Outline each blood parasite and name the species.
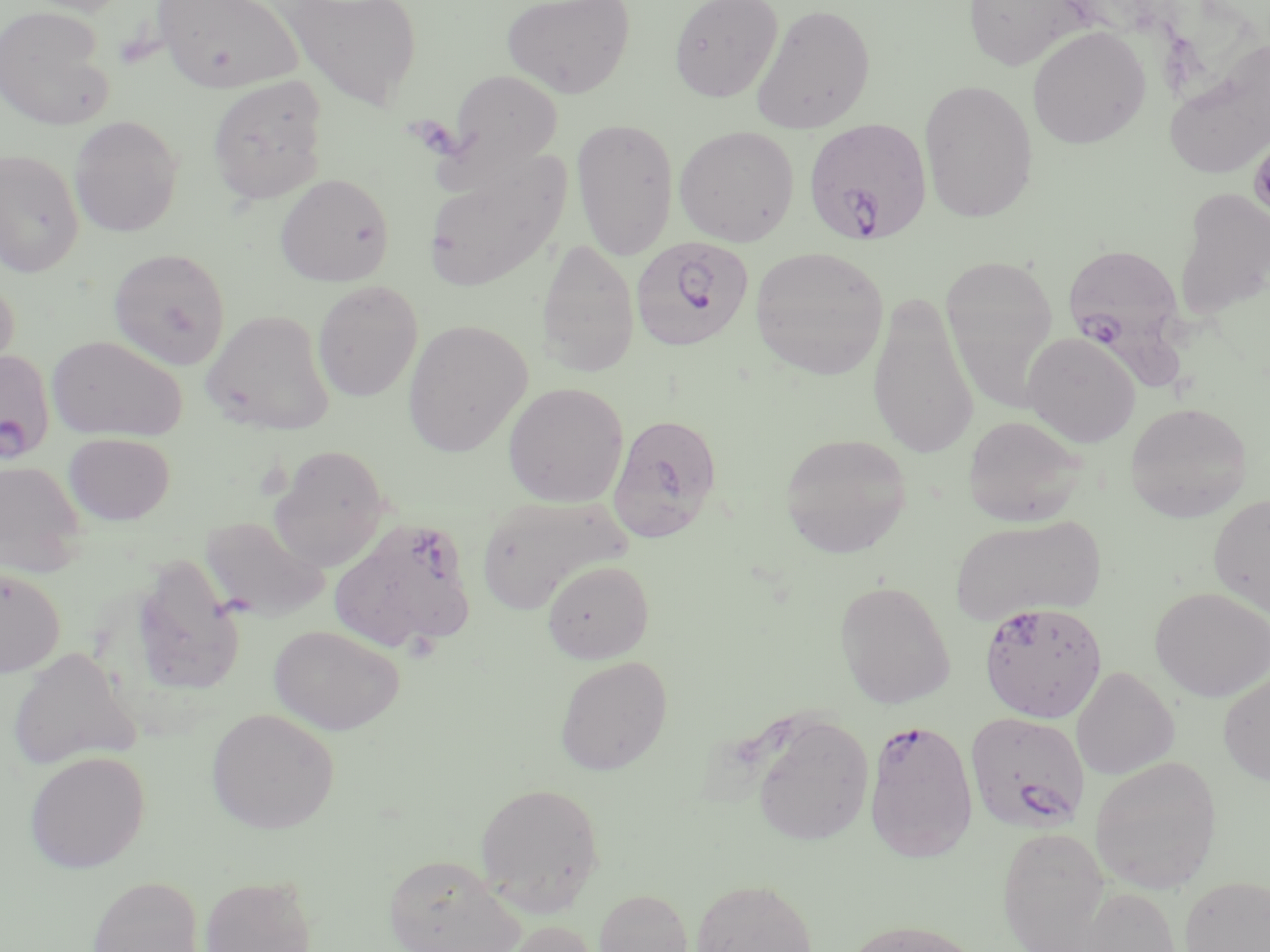
Approximate bounding boxes as named x1/y1/x2/y2 corners in pixels.
Plasmodium falciparum-infected red blood cells: (x1=801, y1=118, x2=937, y2=247), (x1=630, y1=236, x2=755, y2=353), (x1=1061, y1=243, x2=1188, y2=386), (x1=0, y1=350, x2=55, y2=464), (x1=608, y1=413, x2=723, y2=542), (x1=330, y1=517, x2=478, y2=653), (x1=978, y1=601, x2=1108, y2=724), (x1=965, y1=712, x2=1090, y2=834), (x1=863, y1=718, x2=978, y2=862).
No Plasmodium ovale, Plasmodium malariae, Plasmodium vivax, Babesia divergens, or Trypanosoma brucei observed.

Uninfected red blood cell locations: (x1=18, y1=0, x2=132, y2=16), (x1=152, y1=0, x2=305, y2=93), (x1=278, y1=0, x2=424, y2=111), (x1=501, y1=0, x2=635, y2=98), (x1=669, y1=0, x2=784, y2=102), (x1=963, y1=0, x2=1090, y2=71), (x1=750, y1=2, x2=876, y2=134), (x1=0, y1=5, x2=115, y2=131), (x1=1026, y1=25, x2=1151, y2=149), (x1=1164, y1=39, x2=1270, y2=179), (x1=446, y1=69, x2=563, y2=175), (x1=207, y1=75, x2=328, y2=205), (x1=919, y1=79, x2=1039, y2=223), (x1=69, y1=115, x2=183, y2=237), (x1=571, y1=119, x2=680, y2=260), (x1=674, y1=125, x2=800, y2=246), (x1=0, y1=149, x2=85, y2=277), (x1=422, y1=152, x2=570, y2=292), (x1=275, y1=173, x2=394, y2=287), (x1=1173, y1=186, x2=1270, y2=322), (x1=536, y1=237, x2=639, y2=377), (x1=749, y1=246, x2=889, y2=379), (x1=108, y1=248, x2=231, y2=369), (x1=940, y1=253, x2=1059, y2=405), (x1=0, y1=276, x2=20, y2=382), (x1=312, y1=280, x2=423, y2=402), (x1=868, y1=290, x2=979, y2=459), (x1=201, y1=309, x2=336, y2=436), (x1=403, y1=319, x2=532, y2=457), (x1=1022, y1=332, x2=1141, y2=447), (x1=47, y1=334, x2=187, y2=442), (x1=503, y1=382, x2=628, y2=507), (x1=1125, y1=402, x2=1252, y2=523), (x1=963, y1=414, x2=1087, y2=527), (x1=63, y1=432, x2=175, y2=526), (x1=779, y1=433, x2=912, y2=558), (x1=268, y1=444, x2=392, y2=570), (x1=0, y1=458, x2=88, y2=577), (x1=476, y1=494, x2=631, y2=615), (x1=1208, y1=494, x2=1270, y2=618), (x1=949, y1=514, x2=1106, y2=626), (x1=199, y1=516, x2=330, y2=622), (x1=129, y1=556, x2=246, y2=698), (x1=542, y1=559, x2=654, y2=664), (x1=0, y1=566, x2=66, y2=677), (x1=834, y1=579, x2=955, y2=709), (x1=1150, y1=587, x2=1270, y2=701), (x1=268, y1=625, x2=404, y2=734), (x1=7, y1=647, x2=141, y2=770), (x1=555, y1=655, x2=673, y2=775), (x1=1071, y1=667, x2=1179, y2=780), (x1=1217, y1=670, x2=1270, y2=785), (x1=206, y1=708, x2=340, y2=834), (x1=749, y1=712, x2=874, y2=846), (x1=24, y1=750, x2=150, y2=873), (x1=1089, y1=755, x2=1222, y2=893), (x1=475, y1=782, x2=604, y2=914), (x1=997, y1=826, x2=1113, y2=951), (x1=382, y1=854, x2=526, y2=952), (x1=198, y1=874, x2=318, y2=952), (x1=85, y1=875, x2=205, y2=952), (x1=1180, y1=875, x2=1270, y2=952), (x1=691, y1=878, x2=818, y2=951), (x1=1068, y1=886, x2=1183, y2=951), (x1=594, y1=888, x2=694, y2=952), (x1=840, y1=919, x2=987, y2=952), (x1=498, y1=920, x2=603, y2=952). Slide-level diagnosis: Plasmodium falciparum. Image is 1270×952 pixels. 1000x magnification. Optical microscopy. Thin blood smear. One field of a larger specimen. May-Grünwald-Giemsa-stained preparation.